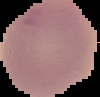
Summary:
  - Malaria status: uninfected
  - Image type: segmented cell region on a black background
  - Image size: 100×97 pixels
  - Preparation: thin blood smear